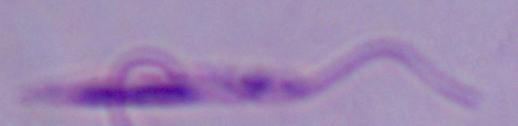
Summary:
  - Magnification: 1000x
  - Modality: photomicrograph
  - Identification: Leishmania